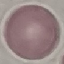

Summary:
  - Malaria status: uninfected
  - Preparation: thin blood smear
  - Stain: Giemsa
  - Capture: smartphone through the microscope eyepiece
  - Image type: automatically extracted cell patch, resized to 64 × 64 pixels